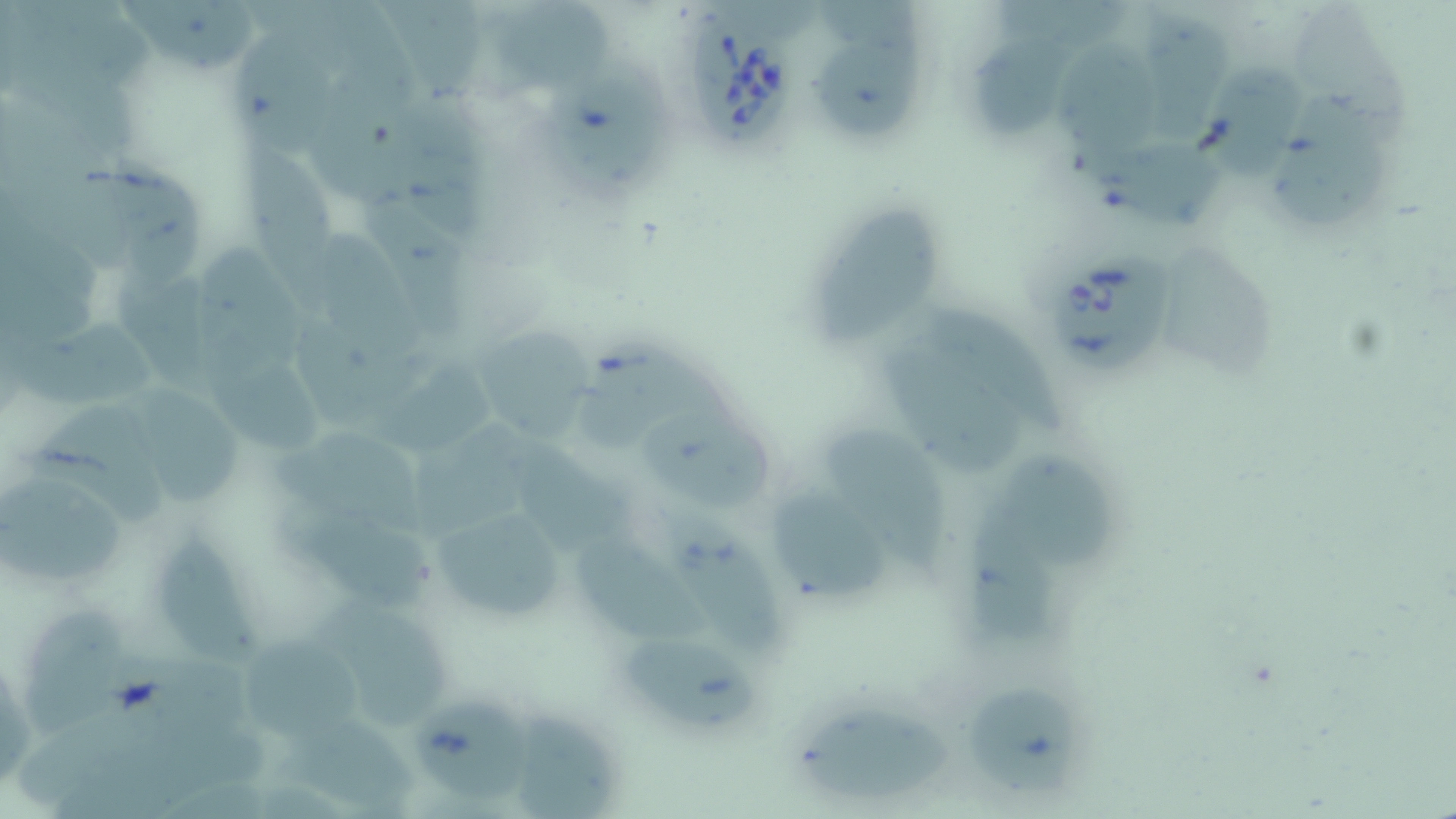 Approximate bounding boxes as (x1, y1, x2, y2) in pixels. Babesia divergens-infected red blood cell locations: (685, 14, 796, 153), (1054, 247, 1175, 372). Uninfected red blood cell locations: (117, 0, 268, 71), (374, 2, 484, 103), (491, 5, 618, 103), (1126, 8, 1235, 153), (235, 31, 342, 159), (968, 33, 1083, 133), (1060, 37, 1162, 164), (812, 43, 924, 141), (1199, 56, 1308, 185), (550, 63, 680, 204), (1266, 91, 1400, 237), (387, 98, 495, 245), (1095, 138, 1231, 235), (241, 141, 346, 312), (111, 159, 212, 296), (361, 183, 473, 342), (807, 201, 949, 347), (1172, 242, 1275, 380), (200, 245, 318, 375), (916, 301, 1072, 441), (12, 318, 165, 414), (474, 325, 591, 441), (575, 332, 757, 460), (197, 338, 328, 453), (883, 338, 1024, 480), (374, 362, 488, 453), (126, 390, 252, 507), (29, 403, 173, 530), (647, 417, 779, 509), (409, 425, 554, 542), (272, 427, 437, 528), (828, 432, 957, 579), (515, 440, 646, 555), (993, 446, 1117, 578), (1, 478, 141, 583), (774, 496, 892, 599), (429, 503, 571, 630), (967, 503, 1060, 641), (290, 512, 440, 614), (664, 515, 791, 656), (161, 528, 265, 662), (576, 533, 716, 649), (318, 594, 458, 737), (23, 604, 135, 747), (243, 630, 373, 749), (626, 630, 763, 737), (963, 688, 1085, 799), (410, 700, 548, 806), (504, 704, 622, 819), (796, 706, 957, 803), (275, 721, 424, 818). Slide-level diagnosis: Babesia divergens. Image is 1456×819 pixels. Captured at 1000x magnification. May-Grünwald-Giemsa stain. Single field of view. Light microscopy. Thin blood smear.